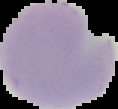

Summary:
  - Image type: segmented cell region on a black background
  - Result: negative for malaria parasites
  - Preparation: thin blood film
  - Image size: 118×109 pixels